Outline each blood parasite and name the species.
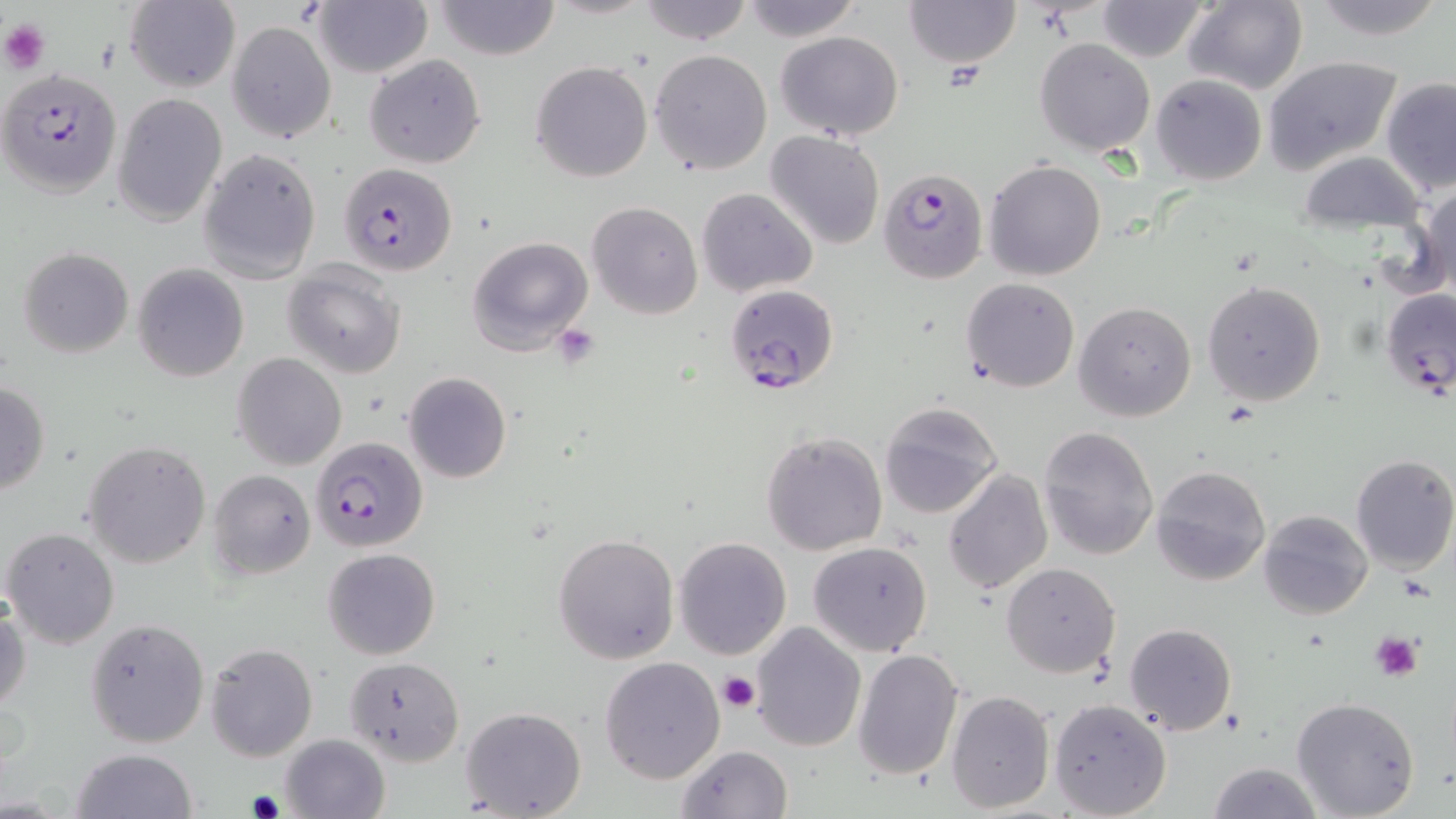
Approximate bounding boxes as (x1, y1, x2, y2) in pixels.
Plasmodium falciparum-infected red blood cells: (1, 69, 122, 195), (337, 162, 458, 277), (878, 167, 989, 283), (724, 283, 840, 394), (1379, 287, 1456, 403), (311, 436, 428, 555).
No Plasmodium ovale, Plasmodium malariae, Plasmodium vivax, Babesia divergens, or Trypanosoma brucei observed.

Summary:
  - Platelet locations: (0, 18, 48, 74), (552, 324, 601, 368), (1370, 632, 1423, 681), (718, 672, 762, 713)
  - Uninfected red blood cell locations: (123, 0, 240, 93), (637, 0, 752, 47), (740, 0, 862, 42), (902, 0, 1019, 68), (1184, 0, 1308, 95), (1308, 0, 1446, 41), (437, 1, 560, 61), (314, 2, 432, 78), (1097, 2, 1206, 60), (227, 22, 337, 145), (776, 30, 904, 141), (1034, 37, 1155, 156), (649, 48, 774, 176), (364, 55, 486, 169), (1263, 56, 1403, 174), (531, 61, 653, 183), (1151, 74, 1267, 186), (1381, 76, 1456, 195), (113, 92, 227, 227), (766, 129, 886, 250), (198, 147, 322, 283), (1298, 149, 1427, 233), (984, 159, 1108, 280), (1412, 184, 1456, 299), (697, 187, 817, 296), (588, 200, 703, 320), (468, 236, 594, 358), (18, 246, 134, 357), (133, 264, 249, 383), (284, 264, 406, 378), (960, 276, 1080, 393), (1202, 280, 1327, 407), (1073, 300, 1197, 422), (232, 352, 346, 471), (402, 371, 512, 484), (0, 380, 50, 496), (878, 401, 1003, 519), (1037, 425, 1159, 559), (760, 430, 889, 556), (84, 440, 211, 569), (1350, 454, 1456, 576), (1151, 464, 1271, 585), (207, 469, 316, 579), (943, 469, 1052, 596), (1259, 508, 1371, 621), (5, 526, 120, 648), (552, 532, 679, 666), (673, 535, 792, 660), (808, 540, 933, 657), (322, 547, 440, 660), (1002, 562, 1120, 679), (0, 600, 30, 715), (85, 617, 210, 748), (1123, 622, 1236, 736), (751, 623, 866, 753), (206, 643, 317, 762), (852, 648, 964, 780), (343, 655, 465, 764), (600, 657, 724, 784), (946, 689, 1055, 813), (1289, 697, 1421, 819), (1048, 698, 1171, 818), (461, 706, 585, 819), (280, 734, 390, 819), (676, 745, 792, 819), (69, 747, 198, 819), (1206, 760, 1323, 819)
  - Slide-level diagnosis: Plasmodium falciparum
  - Field of view: one of a larger specimen
  - Stain: May-Grünwald-Giemsa
  - Image size: 1456×819 pixels
  - Preparation: thin blood film
  - Modality: light microscopy
  - Magnification: 1000x